Name the parasite shown.
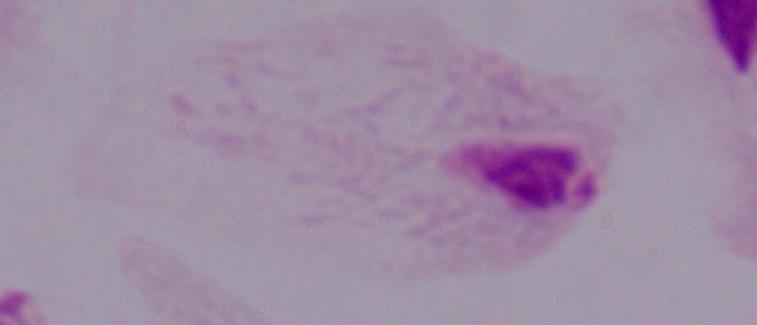
A trichomonad.

magnification = 1000x
modality = photomicrograph